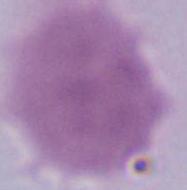
magnification: 1000x
modality: photomicrograph
identification: erythrocyte